Locate every blood parasite and identify its species.
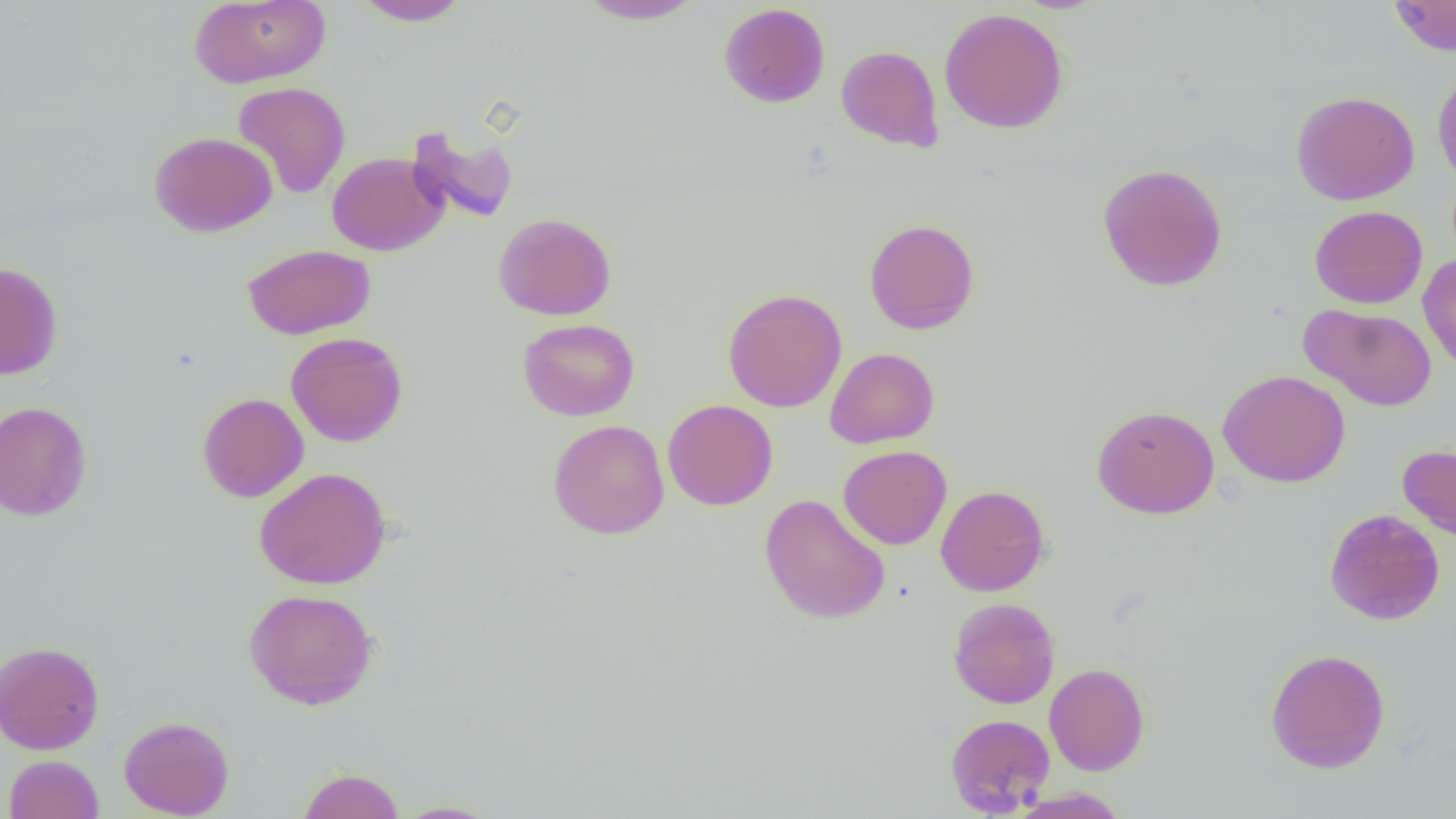

No blood parasites observed.

Summary:
  - Coordinate format: approximate bounding boxes as [x1, y1, x2, y2] in pixels
  - Uninfected red blood cell locations: [189, 0, 331, 88], [352, 0, 472, 26], [575, 0, 706, 25], [1388, 0, 1456, 56], [718, 3, 831, 108], [939, 7, 1069, 134], [836, 45, 944, 151], [1433, 67, 1456, 189], [232, 82, 351, 199], [1291, 90, 1420, 206], [406, 125, 519, 225], [149, 131, 278, 237], [326, 152, 448, 256], [1097, 162, 1228, 291], [1309, 205, 1428, 309], [493, 213, 616, 320], [864, 218, 980, 334], [242, 244, 376, 340], [1418, 253, 1456, 374], [0, 262, 63, 380], [722, 288, 847, 413], [1300, 303, 1437, 412], [518, 318, 640, 421], [286, 332, 408, 447], [825, 347, 939, 448], [1217, 369, 1350, 487], [197, 393, 308, 502], [662, 399, 778, 511], [0, 401, 92, 521], [1091, 404, 1219, 519], [548, 420, 669, 540], [1397, 444, 1456, 541], [838, 445, 951, 549], [253, 467, 391, 589], [936, 484, 1050, 596], [759, 494, 890, 624], [1324, 508, 1445, 625], [243, 588, 379, 709], [948, 597, 1060, 709], [0, 640, 104, 755], [1265, 648, 1390, 773], [1044, 663, 1149, 775], [945, 713, 1055, 816], [119, 715, 234, 818], [4, 754, 104, 819], [297, 767, 405, 819], [1011, 787, 1130, 819], [393, 800, 501, 818]
  - Slide-level diagnosis: negative for blood parasites
  - Image size: 1456×819 pixels
  - Field of view: one of a larger specimen
  - Magnification: 1000x
  - Modality: optical microscopy
  - Preparation: thin blood film